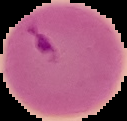
preparation: thin blood film
malaria_status: parasitized
image_type: segmented cell region with the area outside set to black
image_size: 127×121 pixels